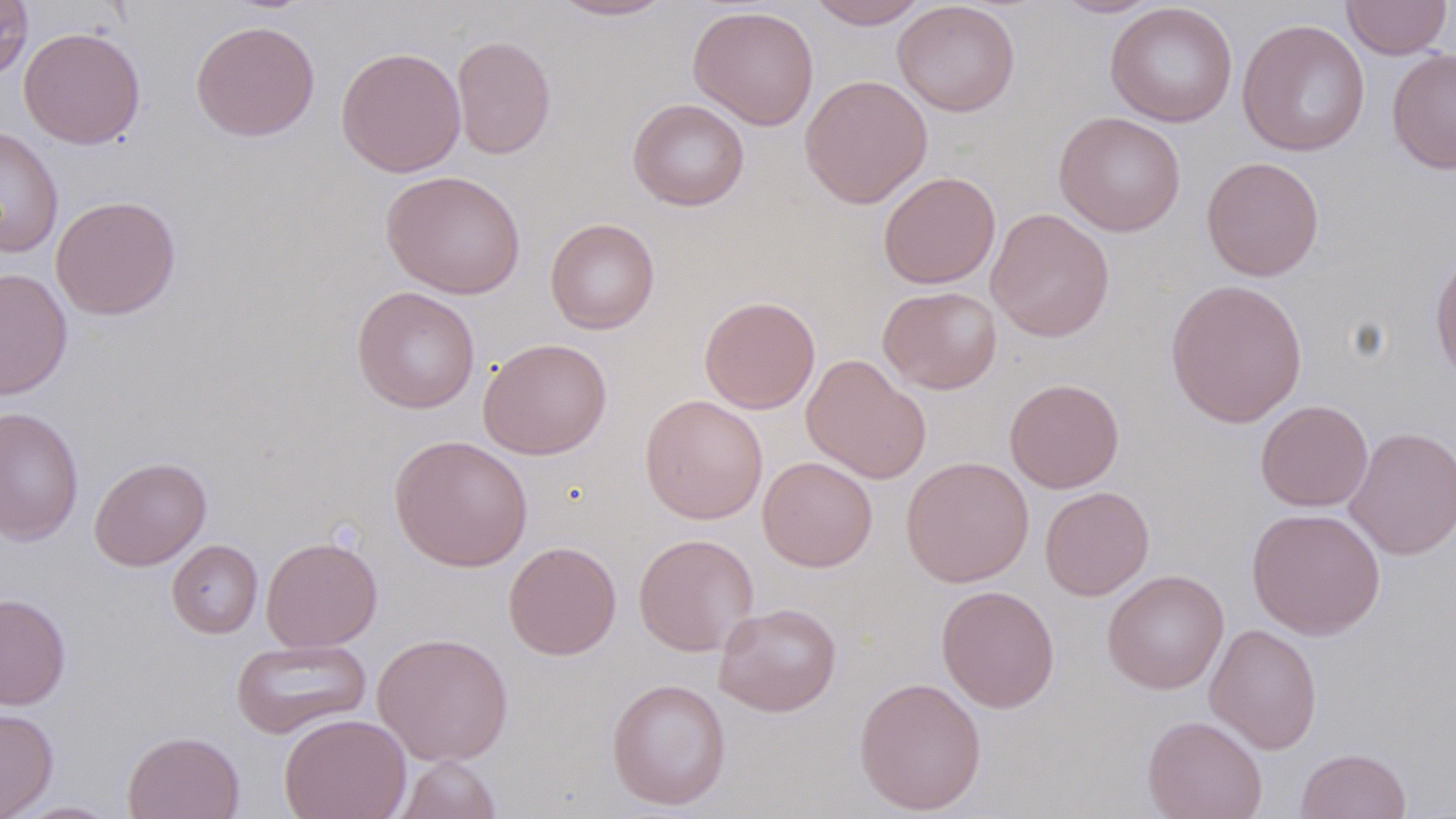

Summary:
  - Coordinate format: approximate bounding boxes as (x1, y1, x2, y2) in pixels
  - Uninfected red blood cell locations: (0, 0, 34, 82), (549, 0, 675, 21), (805, 0, 929, 29), (1050, 0, 1164, 18), (1341, 0, 1452, 60), (892, 1, 1020, 117), (1105, 2, 1238, 127), (688, 5, 820, 131), (1236, 18, 1371, 157), (190, 20, 320, 142), (18, 26, 147, 149), (451, 35, 556, 160), (336, 46, 466, 178), (1387, 47, 1456, 176), (799, 74, 933, 208), (627, 98, 750, 211), (1053, 111, 1185, 236), (0, 126, 63, 258), (1202, 156, 1324, 281), (380, 170, 526, 299), (878, 171, 1001, 289), (50, 195, 181, 320), (986, 208, 1115, 343), (545, 217, 660, 334), (1430, 248, 1456, 385), (0, 268, 73, 400), (1165, 277, 1308, 427), (351, 286, 480, 414), (878, 286, 1003, 395), (699, 296, 821, 414), (478, 338, 613, 460), (801, 355, 931, 484), (1004, 378, 1124, 493), (640, 394, 768, 524), (1255, 400, 1373, 512), (0, 406, 84, 546), (1344, 426, 1456, 560), (389, 434, 533, 572), (89, 456, 212, 571), (757, 456, 877, 572), (901, 456, 1034, 587), (1039, 486, 1154, 601), (1246, 507, 1386, 641), (633, 533, 758, 656), (261, 537, 383, 652), (167, 539, 263, 638), (503, 541, 622, 660), (1102, 569, 1229, 694), (936, 584, 1060, 713), (0, 593, 72, 710), (713, 602, 842, 717), (1205, 624, 1322, 755), (372, 632, 514, 767), (231, 638, 372, 739), (853, 676, 987, 815), (606, 678, 731, 810), (0, 707, 59, 818), (279, 713, 412, 819), (1142, 714, 1268, 819), (123, 730, 245, 819), (1295, 748, 1411, 819), (393, 756, 504, 819), (9, 800, 124, 818)
  - Slide-level diagnosis: negative for blood parasites
  - Field of view: single
  - Modality: light microscopy
  - Image size: 1456×819 pixels
  - Magnification: 1000x
  - Preparation: thin blood film
  - Stain: May-Grünwald-Giemsa